Locate every Trypanosoma brucei.
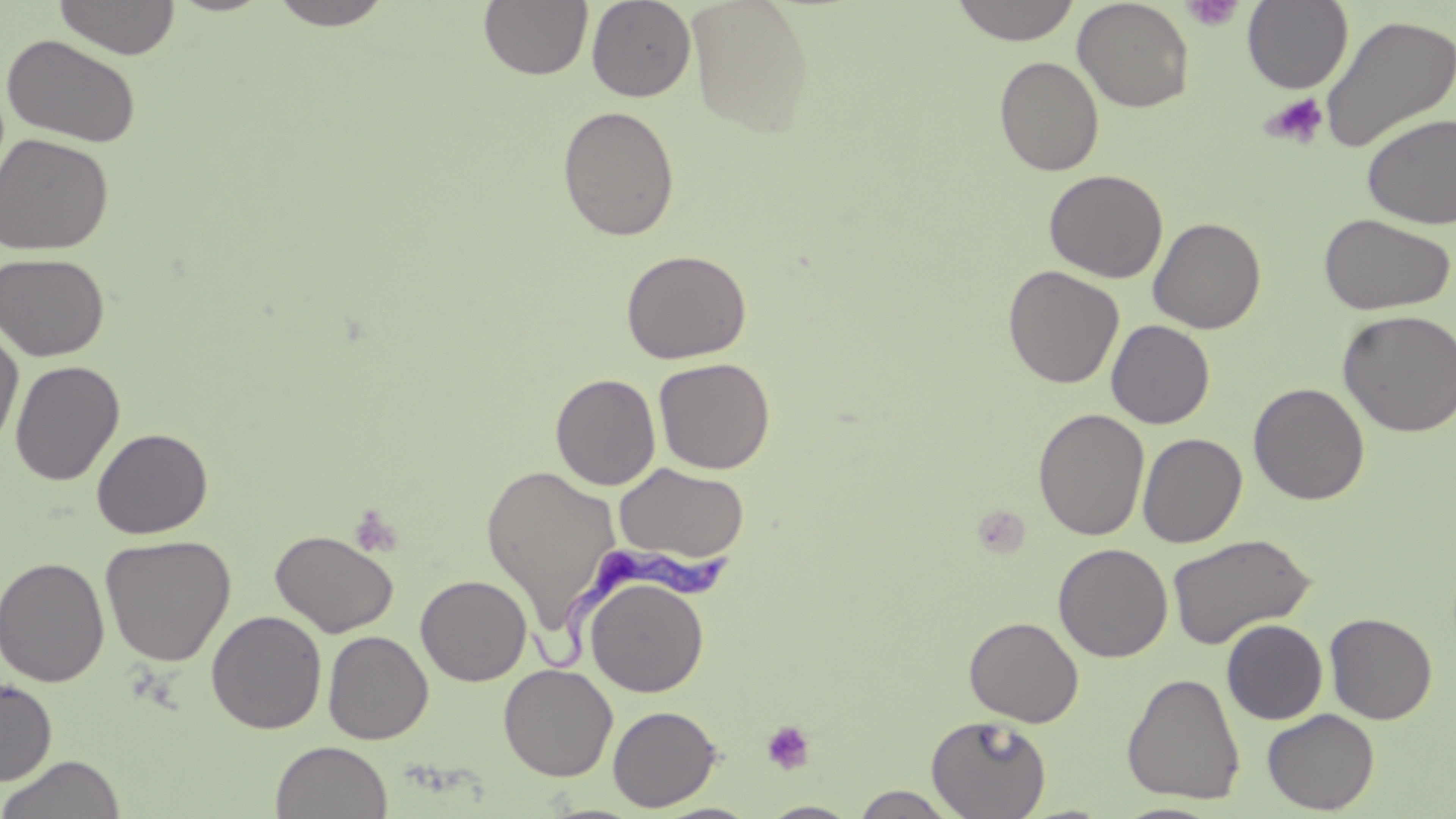
Approximate bounding boxes as (x1, y1, x2, y2) in pixels.
Trypanosoma brucei: (520, 540, 732, 673).

slide_level_diagnosis: Trypanosoma brucei
stain: May-Grünwald-Giemsa
magnification: 1000x
preparation: thin blood film
platelet_locations: 'approximate bounding boxes as (x1, y1, x2, y2) in pixels: (1181, 0, 1244, 31), (1259, 92, 1329, 149), (348, 503, 404, 557), (761, 720, 817, 775)'
uninfected_red_blood_cell_locations: 'approximate bounding boxes as (x1, y1, x2, y2) in pixels: (53, 0, 181, 60), (267, 0, 394, 30), (586, 0, 696, 101), (686, 0, 816, 137), (950, 0, 1081, 45), (1072, 0, 1194, 112), (1242, 0, 1354, 93), (479, 1, 593, 81), (1319, 13, 1456, 154), (1, 33, 141, 149), (994, 56, 1105, 176), (557, 105, 680, 241), (1361, 114, 1456, 230), (0, 133, 114, 256), (1044, 169, 1168, 283), (1318, 213, 1455, 316), (1148, 217, 1266, 334), (621, 249, 752, 364), (0, 252, 110, 361), (1003, 265, 1124, 389), (1337, 309, 1456, 437), (1106, 320, 1215, 429), (0, 325, 24, 453), (653, 357, 775, 474), (9, 360, 124, 486), (550, 372, 661, 491), (1248, 382, 1370, 505), (1033, 408, 1150, 541), (92, 427, 213, 539), (1137, 432, 1247, 548), (613, 462, 749, 564), (480, 463, 622, 631), (269, 529, 398, 638), (1166, 533, 1316, 649), (100, 534, 236, 666), (1053, 542, 1173, 663), (0, 556, 110, 688), (415, 574, 532, 686), (585, 575, 709, 697), (206, 610, 327, 734), (1324, 613, 1438, 724), (964, 616, 1084, 728), (1221, 619, 1327, 724), (323, 630, 433, 744), (498, 663, 618, 781), (1122, 672, 1246, 804), (0, 679, 57, 786), (607, 705, 721, 812), (1262, 708, 1380, 814), (926, 715, 1052, 818), (270, 741, 393, 819), (0, 754, 126, 819), (851, 786, 961, 818), (760, 801, 862, 818)'
modality: light microscopy
image_size: 1456×819 pixels
field_of_view: single